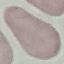
Malaria status: uninfected. Thin smear of blood. Acquired by smartphone through the microscope eyepiece. Giemsa stain. Automatically extracted cell patch, resized to 64 × 64 pixels.